Outline each blood parasite and name the species.
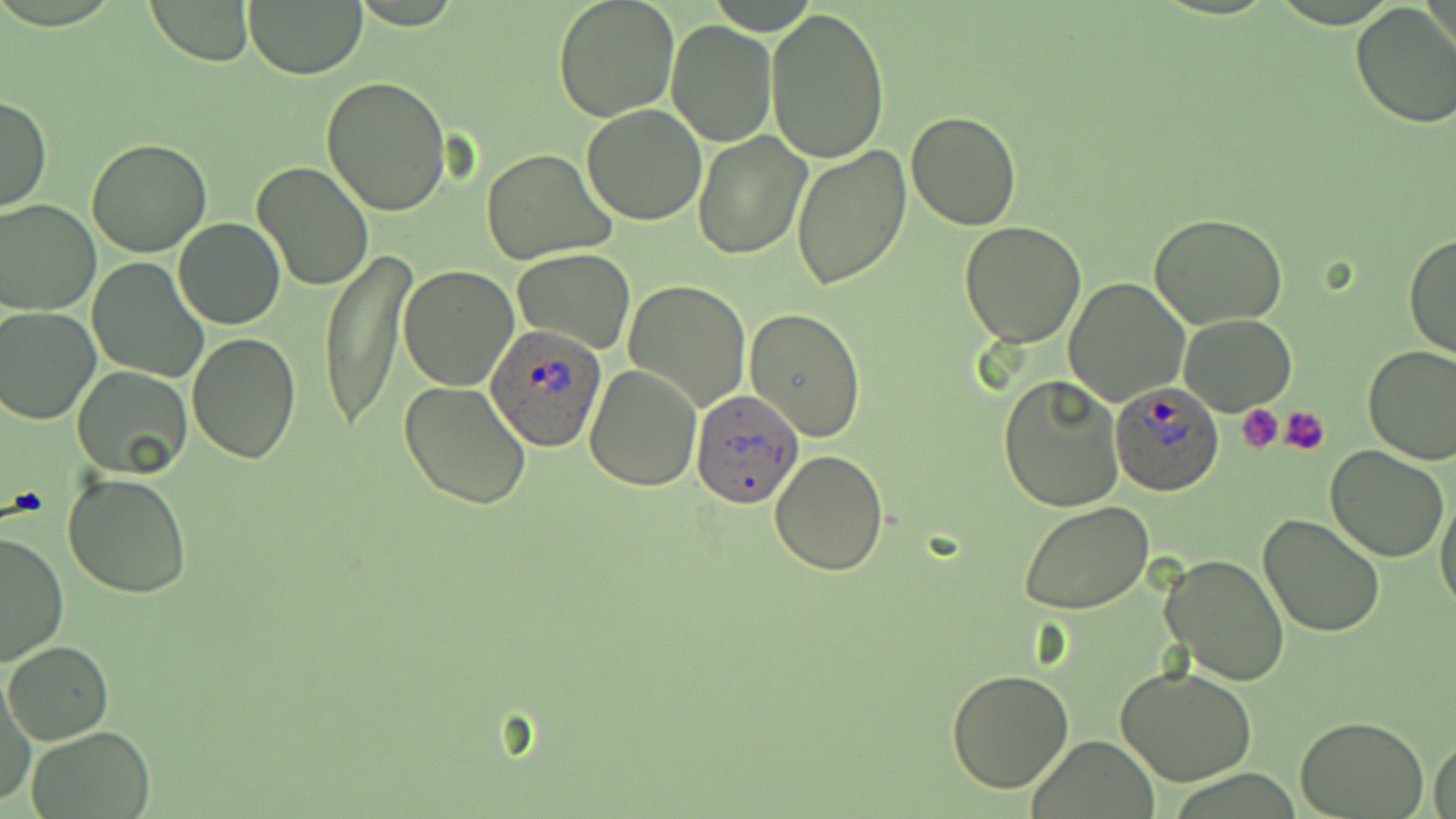

Approximate bounding boxes as named x1/y1/x2/y2 corners in pixels.
Plasmodium ovale-infected red blood cells: (x1=485, y1=328, x2=609, y2=454), (x1=1110, y1=381, x2=1225, y2=496), (x1=691, y1=386, x2=801, y2=512).
No Plasmodium falciparum, Plasmodium malariae, Plasmodium vivax, Babesia divergens, or Trypanosoma brucei observed.

Uninfected red blood cell locations: (x1=142, y1=0, x2=254, y2=65), (x1=243, y1=0, x2=366, y2=79), (x1=553, y1=0, x2=680, y2=122), (x1=1348, y1=2, x2=1456, y2=130), (x1=766, y1=6, x2=891, y2=165), (x1=666, y1=20, x2=777, y2=146), (x1=322, y1=75, x2=454, y2=216), (x1=0, y1=93, x2=52, y2=214), (x1=583, y1=105, x2=706, y2=225), (x1=906, y1=110, x2=1022, y2=231), (x1=692, y1=130, x2=813, y2=262), (x1=86, y1=137, x2=213, y2=258), (x1=790, y1=146, x2=911, y2=289), (x1=481, y1=147, x2=616, y2=265), (x1=250, y1=162, x2=374, y2=292), (x1=0, y1=199, x2=99, y2=315), (x1=1150, y1=212, x2=1288, y2=329), (x1=174, y1=218, x2=285, y2=330), (x1=958, y1=220, x2=1087, y2=347), (x1=1404, y1=232, x2=1456, y2=361), (x1=321, y1=245, x2=412, y2=430), (x1=513, y1=249, x2=635, y2=352), (x1=88, y1=257, x2=209, y2=383), (x1=399, y1=265, x2=520, y2=391), (x1=1063, y1=277, x2=1189, y2=408), (x1=624, y1=280, x2=751, y2=412), (x1=0, y1=306, x2=100, y2=425), (x1=744, y1=307, x2=866, y2=444), (x1=1179, y1=312, x2=1296, y2=415), (x1=187, y1=330, x2=302, y2=465), (x1=1363, y1=344, x2=1456, y2=464), (x1=73, y1=365, x2=193, y2=478), (x1=584, y1=365, x2=702, y2=493), (x1=999, y1=375, x2=1124, y2=513), (x1=398, y1=379, x2=532, y2=510), (x1=1326, y1=447, x2=1448, y2=563), (x1=770, y1=449, x2=889, y2=576), (x1=64, y1=471, x2=192, y2=599), (x1=1435, y1=488, x2=1456, y2=618), (x1=1021, y1=503, x2=1153, y2=615), (x1=1259, y1=515, x2=1385, y2=639), (x1=1, y1=529, x2=70, y2=667), (x1=1161, y1=553, x2=1290, y2=686), (x1=5, y1=640, x2=114, y2=745), (x1=1116, y1=666, x2=1260, y2=787), (x1=947, y1=669, x2=1076, y2=793), (x1=0, y1=671, x2=36, y2=809), (x1=1297, y1=716, x2=1426, y2=818), (x1=25, y1=726, x2=157, y2=819), (x1=1030, y1=736, x2=1159, y2=817), (x1=1430, y1=737, x2=1456, y2=819). Platelet locations: (x1=1238, y1=404, x2=1283, y2=453), (x1=1280, y1=406, x2=1330, y2=456). Slide-level diagnosis: Plasmodium ovale. May-Grünwald-Giemsa-stained preparation. Light microscopy. Image is 1456×819 pixels. One field of a larger specimen. Thin blood smear. Captured at 1000x magnification.